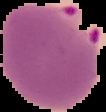
image type = cell region segmented out of the field of view; surrounding area masked to black
image size = 106×112 pixels
preparation = thin blood film
result = malaria parasites detected